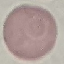
Summary:
  - Result: no malaria parasites seen
  - Image type: automatically extracted cell patch, resized to 64 × 64 pixels
  - Capture: smartphone camera at the microscope eyepiece
  - Preparation: thin blood smear
  - Stain: Giemsa